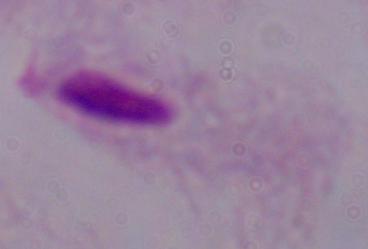
Photomicrograph. Captured at 1000x magnification. A trichomonad is seen.